Identify the parasite.
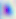
Toxoplasma gondii.

modality = micrograph
magnification = 400x